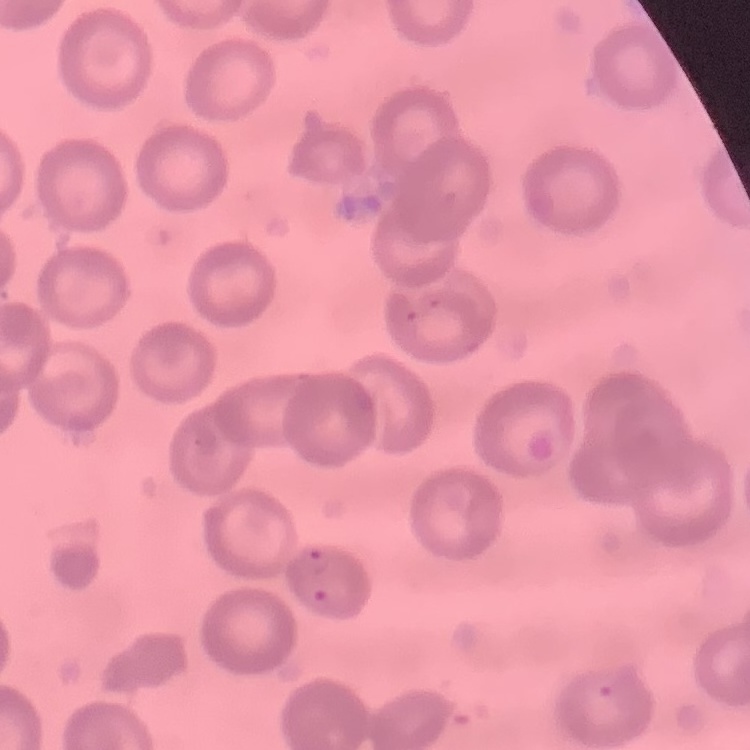 The red blood cells exhibit no rouleaux formation. Stained with either Field's or Giemsa. One tile cut from a larger photomicrograph. Thin blood film.